Assess for malaria.
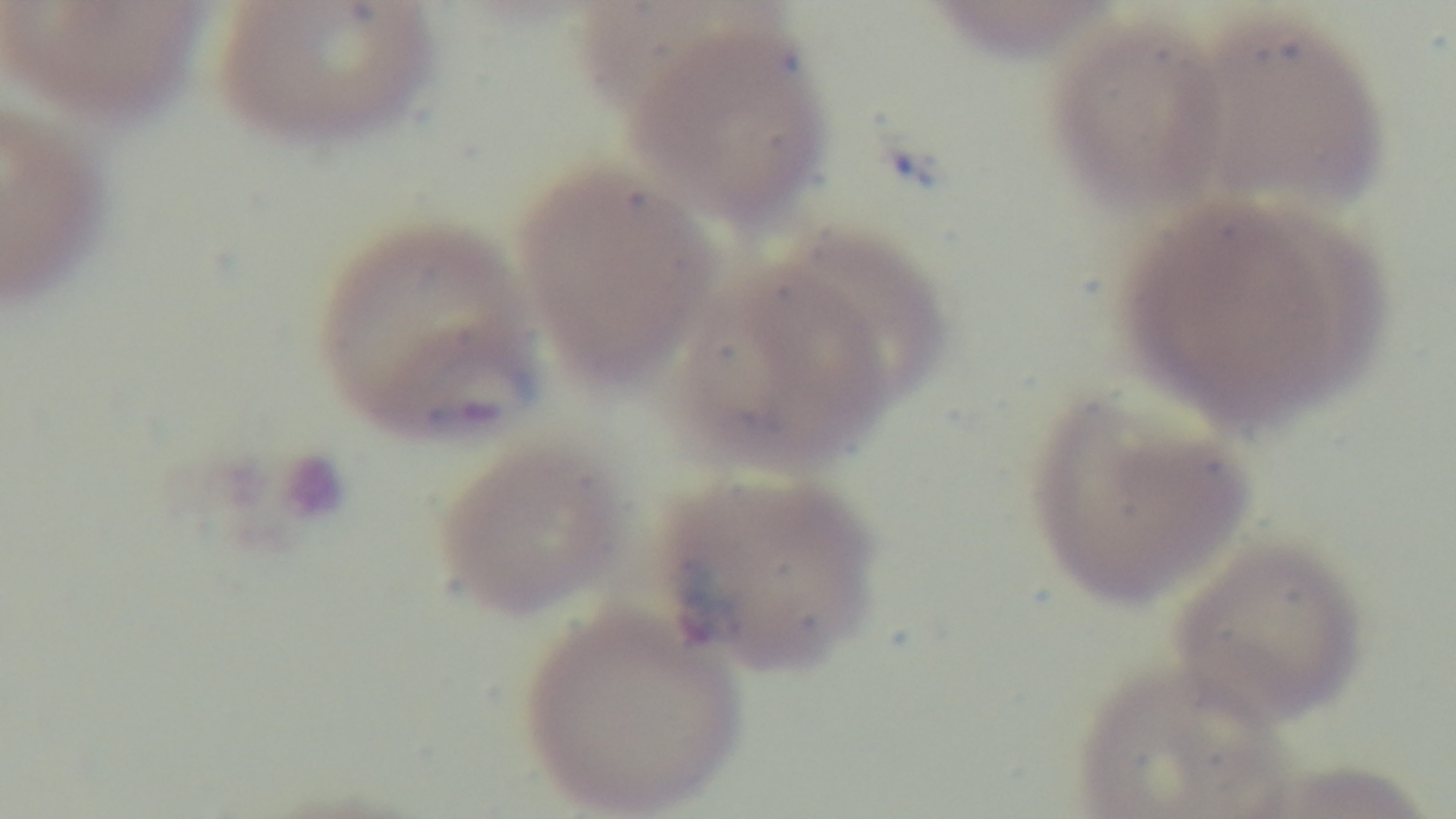

It is infected.

Preparation: thin smear. Captured with a mounted 4K digital camera. One field from the slide. Oil-immersion objective, 100x. Giemsa-stained. Photomicrograph.